Outline each Plasmodium malariae-infected red blood cell.
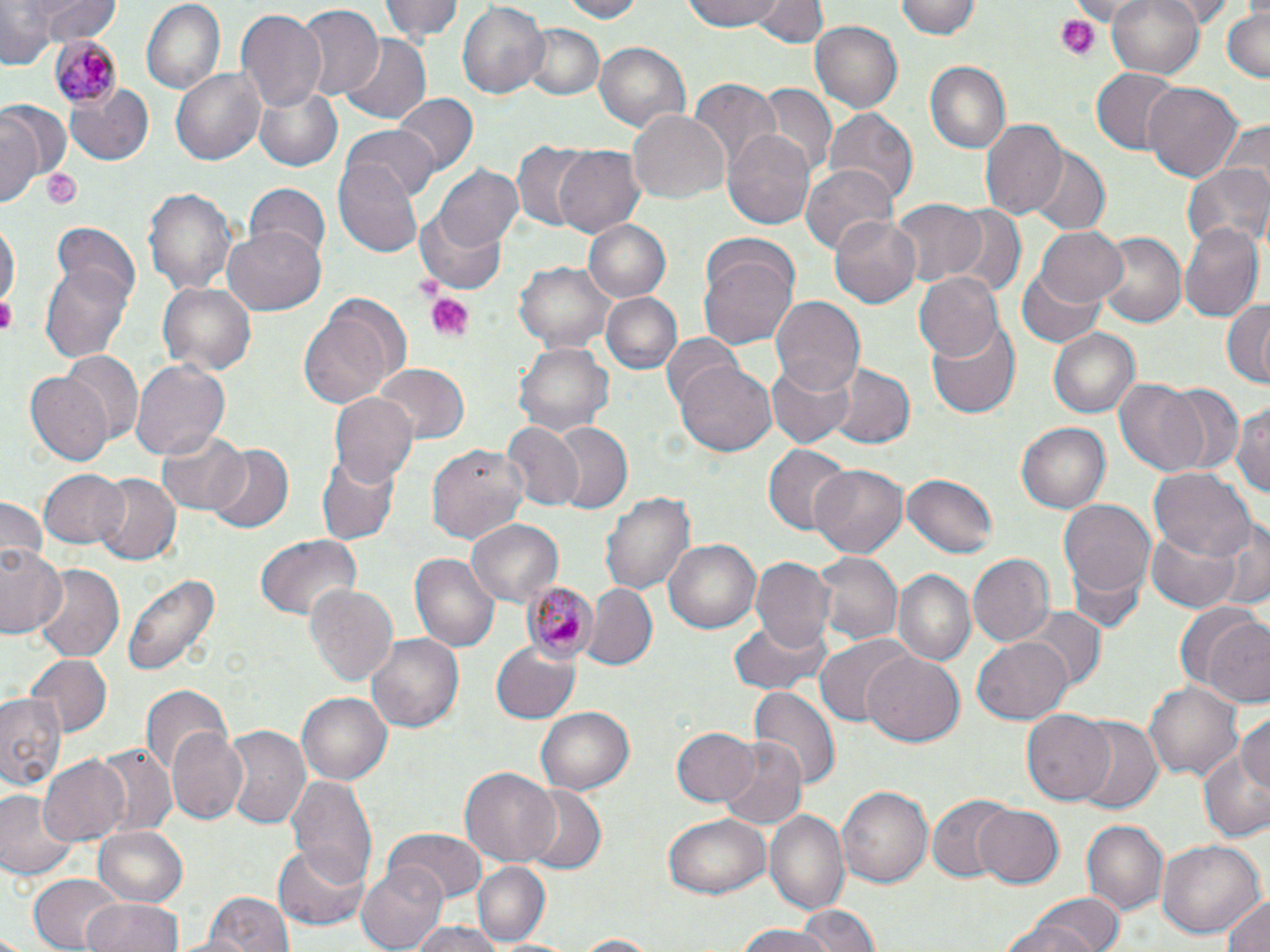
Approximate bounding boxes as (x1, y1, x2, y2) in pixels.
Plasmodium malariae-infected red blood cells: (48, 37, 122, 110), (520, 579, 601, 664).

Summary:
  - Uninfected red blood cell locations: (29, 0, 117, 47), (139, 0, 225, 94), (381, 0, 465, 44), (553, 0, 646, 22), (682, 0, 788, 33), (754, 0, 824, 48), (898, 0, 984, 39), (1105, 0, 1207, 79), (0, 1, 53, 70), (454, 2, 549, 101), (292, 4, 383, 101), (1221, 7, 1269, 84), (235, 9, 326, 114), (809, 20, 904, 115), (520, 24, 604, 101), (340, 34, 432, 124), (595, 41, 689, 135), (925, 61, 1010, 153), (1089, 67, 1179, 154), (171, 68, 267, 167), (687, 78, 780, 173), (1143, 82, 1244, 182), (66, 83, 153, 168), (752, 83, 838, 178), (254, 84, 343, 170), (393, 93, 478, 180), (2, 99, 72, 190), (822, 107, 918, 205), (627, 108, 727, 205), (2, 113, 42, 206), (979, 118, 1068, 221), (343, 125, 439, 204), (722, 128, 815, 230), (512, 140, 601, 231), (553, 144, 645, 237), (1028, 148, 1109, 236), (333, 155, 423, 257), (799, 162, 896, 257), (1184, 162, 1268, 248), (435, 164, 523, 250), (241, 182, 333, 263), (142, 187, 239, 298), (889, 199, 987, 288), (941, 202, 1027, 293), (416, 207, 509, 295), (831, 216, 921, 308), (582, 219, 672, 303), (0, 220, 17, 318), (1180, 221, 1263, 321), (223, 222, 326, 312), (1034, 225, 1129, 308), (1092, 230, 1187, 328), (698, 241, 799, 349), (40, 254, 135, 365), (515, 260, 617, 353), (1017, 261, 1109, 348), (914, 271, 1003, 362), (157, 283, 256, 375), (600, 291, 682, 375), (770, 296, 864, 398), (1221, 297, 1269, 389), (298, 300, 402, 409), (929, 316, 1021, 418), (1049, 327, 1140, 419), (661, 334, 745, 414), (515, 341, 614, 436), (60, 351, 142, 445), (130, 359, 231, 460), (767, 360, 853, 447), (825, 362, 913, 450), (674, 363, 777, 457), (374, 364, 470, 444), (26, 371, 113, 466), (1113, 379, 1212, 474), (1153, 383, 1245, 476), (328, 391, 418, 489), (1233, 398, 1270, 503), (546, 420, 634, 515), (1018, 421, 1110, 515), (501, 422, 584, 512), (154, 428, 250, 515), (202, 444, 294, 533), (428, 444, 530, 549), (763, 445, 850, 535), (316, 451, 398, 548), (810, 461, 910, 559), (1150, 468, 1253, 562), (40, 469, 128, 549), (92, 472, 180, 565), (902, 473, 999, 560), (603, 492, 696, 597), (0, 495, 47, 572), (1058, 499, 1156, 607), (1213, 515, 1269, 613), (466, 518, 563, 608), (1147, 523, 1244, 614), (256, 534, 361, 621), (662, 538, 761, 635), (0, 541, 66, 640), (812, 551, 905, 646), (409, 552, 500, 652), (967, 554, 1052, 649), (749, 557, 836, 655), (32, 563, 126, 661), (894, 568, 975, 667), (121, 571, 220, 679), (306, 583, 399, 687), (582, 585, 657, 673), (1180, 604, 1270, 705), (1020, 607, 1105, 689), (730, 616, 830, 696), (366, 633, 464, 733), (815, 635, 910, 726), (973, 635, 1073, 722), (489, 641, 580, 725), (863, 649, 964, 744), (25, 654, 112, 737), (1146, 681, 1242, 778), (141, 683, 233, 780), (749, 685, 838, 793), (0, 691, 67, 793), (296, 692, 392, 786), (537, 705, 636, 795), (1022, 709, 1116, 806), (1237, 712, 1270, 794), (1074, 719, 1163, 814), (168, 722, 250, 822), (220, 724, 309, 829), (672, 726, 759, 807), (716, 736, 808, 830), (94, 742, 177, 839), (1196, 751, 1270, 842), (38, 754, 133, 845), (458, 767, 560, 865), (287, 775, 378, 890), (836, 784, 932, 891), (520, 788, 607, 876), (0, 789, 77, 881), (926, 793, 1017, 883), (972, 803, 1066, 890), (766, 809, 851, 919), (663, 814, 771, 899), (1081, 820, 1167, 916), (93, 826, 189, 908), (385, 829, 486, 902), (1159, 839, 1264, 939), (272, 842, 370, 933), (472, 861, 553, 946), (356, 864, 449, 951), (26, 874, 125, 952), (198, 889, 297, 952), (1222, 892, 1270, 952), (1017, 893, 1127, 952), (83, 897, 186, 952), (794, 909, 880, 951), (725, 924, 851, 950), (408, 925, 505, 952), (567, 934, 665, 951)
  - Platelet locations: (1053, 16, 1100, 61), (40, 166, 83, 209), (410, 273, 444, 302), (423, 291, 475, 340), (0, 296, 15, 335)
  - Slide-level diagnosis: Plasmodium malariae
  - Field of view: single
  - Stain: May-Grünwald-Giemsa
  - Modality: light microscopy
  - Magnification: 1000x
  - Image size: 1270×952 pixels
  - Preparation: thin blood film